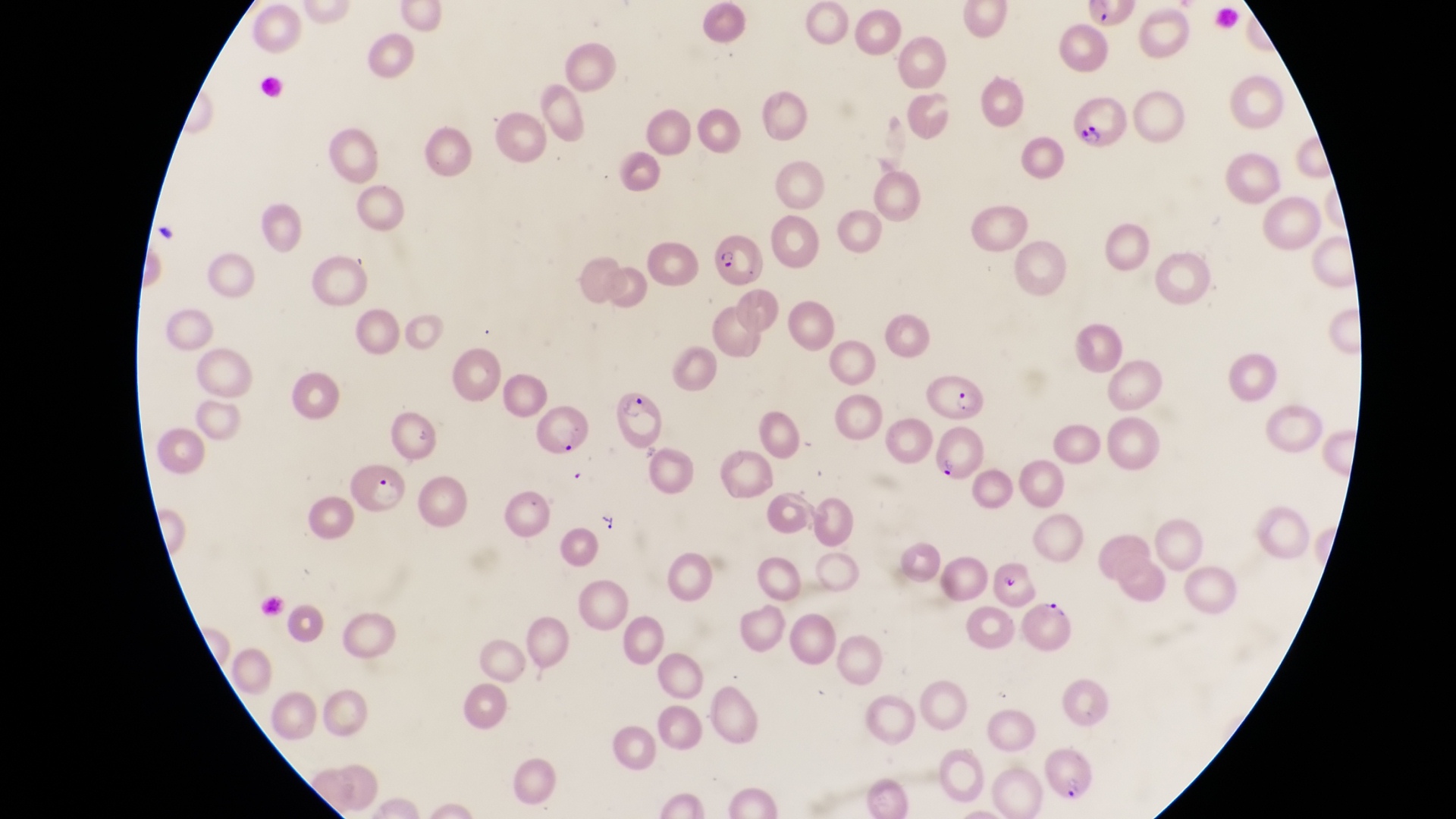
Approximate bounding boxes as left top right bottom in pixels.
Summary:
  - Parasitised red blood cell locations: 1067 95 1126 145; 714 232 772 291; 917 372 990 421; 611 391 664 446; 532 405 595 457; 935 426 985 482; 347 465 411 520; 1028 593 1077 654; 1034 743 1101 806
  - Capture: smartphone photograph through the eyepiece of an Olympus CX-23 microscope
  - Image size: 1456×819 pixels
  - Field of view: single
  - Magnification: 1000x
  - Preparation: thin blood smear
  - Country: Uganda